Locate every leukocyte (white blood cell).
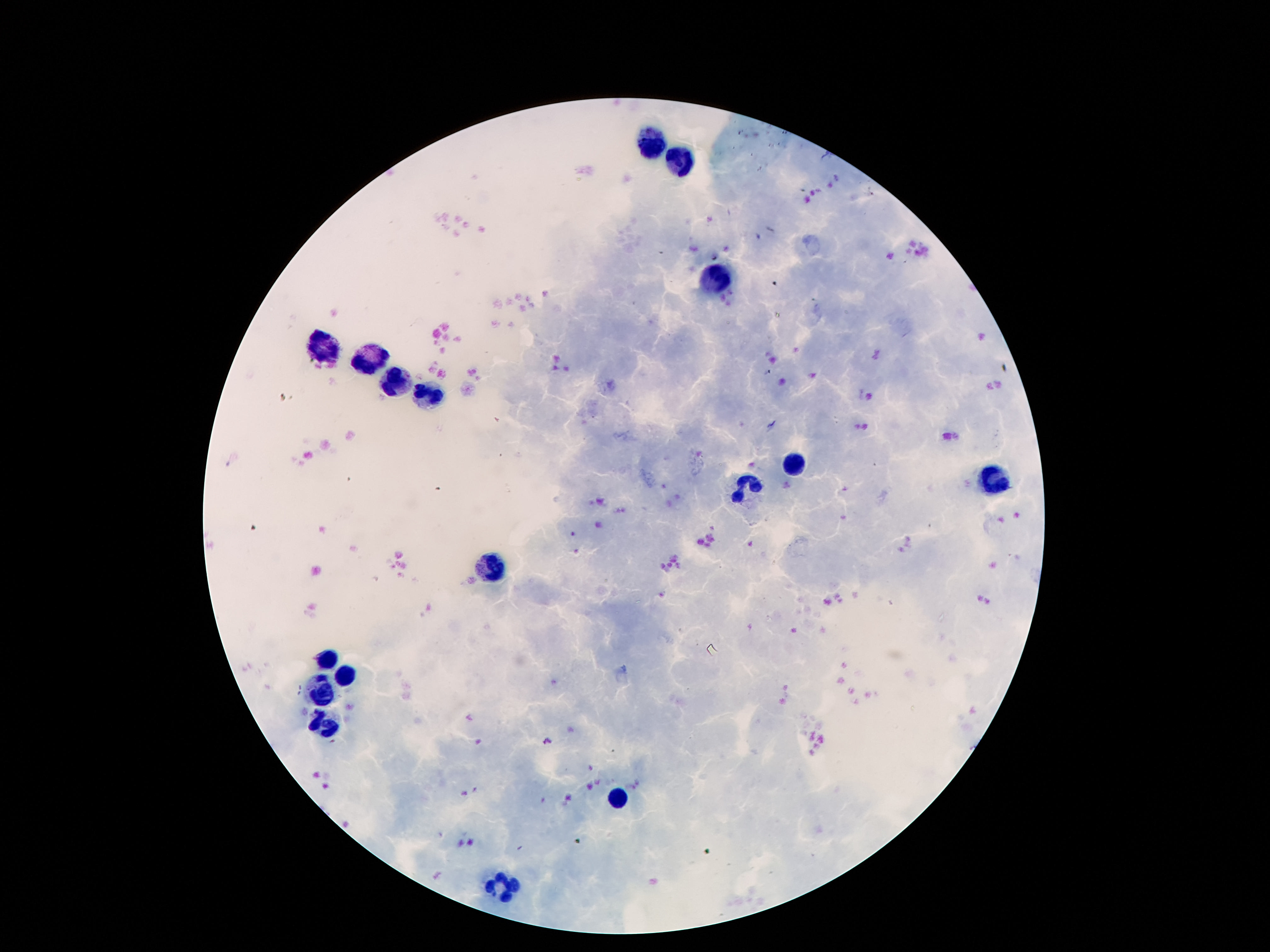
Approximate centers as [x, y] in pixels.
Leukocytes: [652, 136], [682, 163], [716, 277], [319, 342], [371, 361], [394, 385], [428, 395], [793, 463], [995, 478], [750, 483], [491, 567], [328, 658], [348, 674], [319, 692], [321, 723], [616, 800], [503, 884].

Thick peripheral-blood smear. Smartphone photograph taken through the microscope eyepiece. 100x magnification. One field from this slide. Image is 1270×952 pixels. Giemsa-stained preparation. Patient malaria status: uninfected.